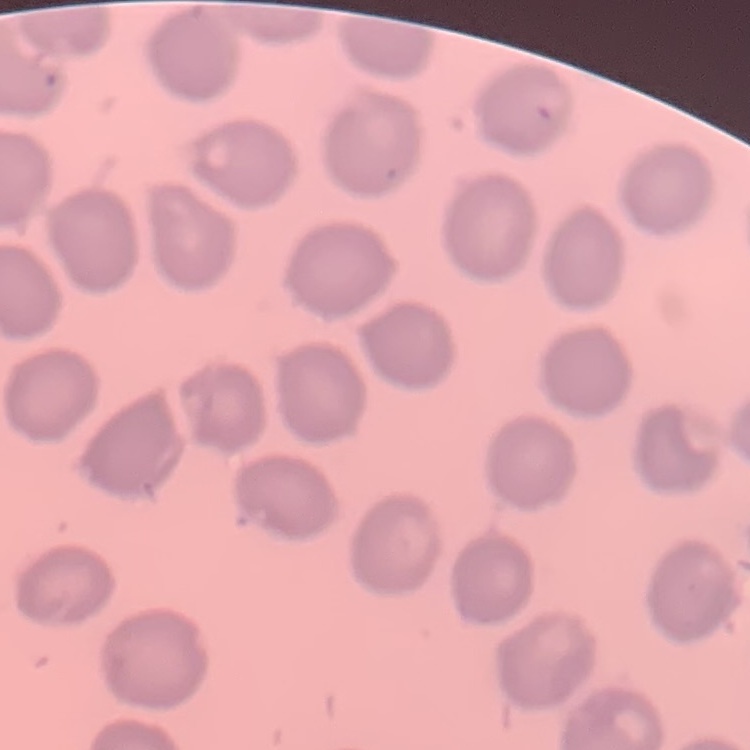
The red blood cells show no rouleaux formation. One tile cut from a larger photomicrograph. Stained with either Field's or Giemsa. Thin blood smear.